Report the malaria status of this cell.
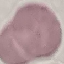
Uninfected.

Summary:
  - Preparation: thin smear
  - Stain: Giemsa
  - Capture: smartphone through the microscope eyepiece
  - Image type: automatically extracted cell patch, resized to 64 × 64 pixels